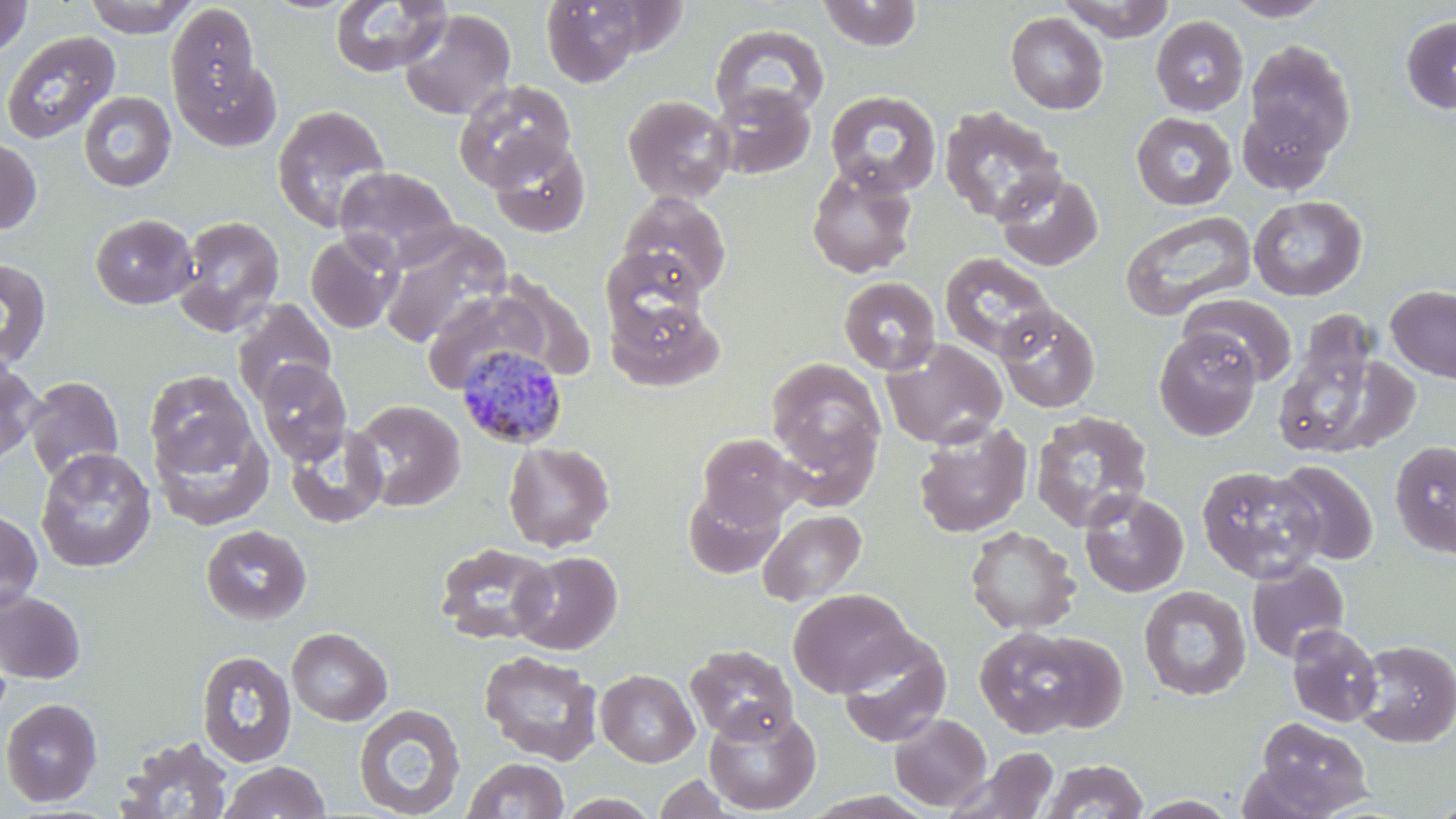
Summary:
  - Coordinate format: approximate bounding boxes as (x1, y1, x2, y2) in pixels
  - Plasmodium malariae-infected red blood cell locations: (457, 345, 569, 450)
  - Uninfected red blood cell locations: (0, 0, 33, 57), (83, 0, 198, 38), (539, 0, 651, 86), (1058, 0, 1176, 42), (329, 1, 452, 77), (817, 1, 923, 51), (1223, 1, 1334, 22), (167, 2, 261, 114), (399, 9, 516, 121), (1005, 12, 1108, 114), (1150, 15, 1249, 116), (1400, 15, 1456, 115), (709, 24, 830, 126), (1, 31, 120, 145), (1245, 41, 1356, 158), (174, 56, 282, 152), (454, 80, 577, 190), (710, 84, 817, 179), (824, 89, 942, 198), (78, 91, 177, 192), (622, 94, 735, 205), (1237, 100, 1335, 195), (272, 105, 392, 233), (939, 105, 1066, 226), (1131, 112, 1237, 210), (0, 137, 41, 235), (487, 139, 591, 238), (806, 164, 917, 278), (334, 166, 460, 270), (995, 171, 1104, 271), (617, 191, 733, 298), (1248, 195, 1368, 301), (1120, 209, 1256, 321), (89, 214, 197, 310), (173, 215, 285, 336), (378, 224, 510, 347), (306, 232, 403, 333), (600, 247, 706, 338), (939, 252, 1056, 361), (0, 258, 53, 370), (839, 277, 941, 375), (1385, 286, 1456, 383), (420, 287, 552, 395), (1181, 294, 1299, 387), (605, 295, 720, 392), (231, 299, 336, 407), (996, 304, 1101, 413), (1276, 321, 1403, 458), (1153, 328, 1262, 441), (881, 338, 1008, 449), (765, 357, 887, 495), (0, 359, 43, 466), (256, 360, 352, 465), (145, 370, 256, 478), (23, 376, 124, 483), (351, 399, 465, 512), (1030, 410, 1153, 533), (150, 413, 274, 531), (912, 419, 1033, 538), (285, 424, 389, 528), (698, 433, 802, 528), (1390, 440, 1456, 558), (503, 441, 615, 552), (35, 447, 157, 573), (1274, 460, 1379, 566), (1196, 465, 1325, 583), (682, 485, 785, 580), (1078, 489, 1189, 598), (0, 508, 43, 615), (758, 508, 866, 606), (201, 525, 312, 626), (964, 526, 1080, 635), (434, 542, 557, 645), (512, 551, 622, 655), (1246, 560, 1350, 663), (1138, 586, 1252, 701), (788, 588, 915, 696), (0, 590, 86, 684), (1286, 624, 1383, 727), (974, 626, 1118, 739), (287, 627, 392, 726), (836, 630, 951, 747), (1353, 639, 1455, 747), (686, 644, 798, 744), (196, 650, 298, 767), (479, 651, 603, 765), (596, 669, 700, 767), (0, 698, 103, 806), (354, 703, 466, 817), (703, 704, 821, 815), (889, 713, 991, 811), (1253, 716, 1372, 817), (116, 735, 234, 818), (957, 747, 1061, 818), (462, 757, 570, 818), (1039, 759, 1149, 818), (218, 761, 331, 819), (653, 774, 735, 818)
  - Slide-level diagnosis: Plasmodium malariae
  - Preparation: thin blood film
  - Magnification: 1000x
  - Stain: May-Grünwald-Giemsa
  - Field of view: single
  - Modality: optical microscopy
  - Image size: 1456×819 pixels